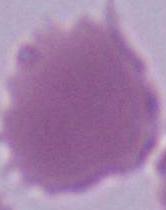
Photomicrograph. A red blood cell is shown. 1000x magnification.